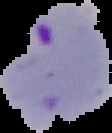

Image is 112×133 pixels. The area outside the segmented cell region is set to black. Malaria status: parasitized. From a thin blood film.